State the preparation type.
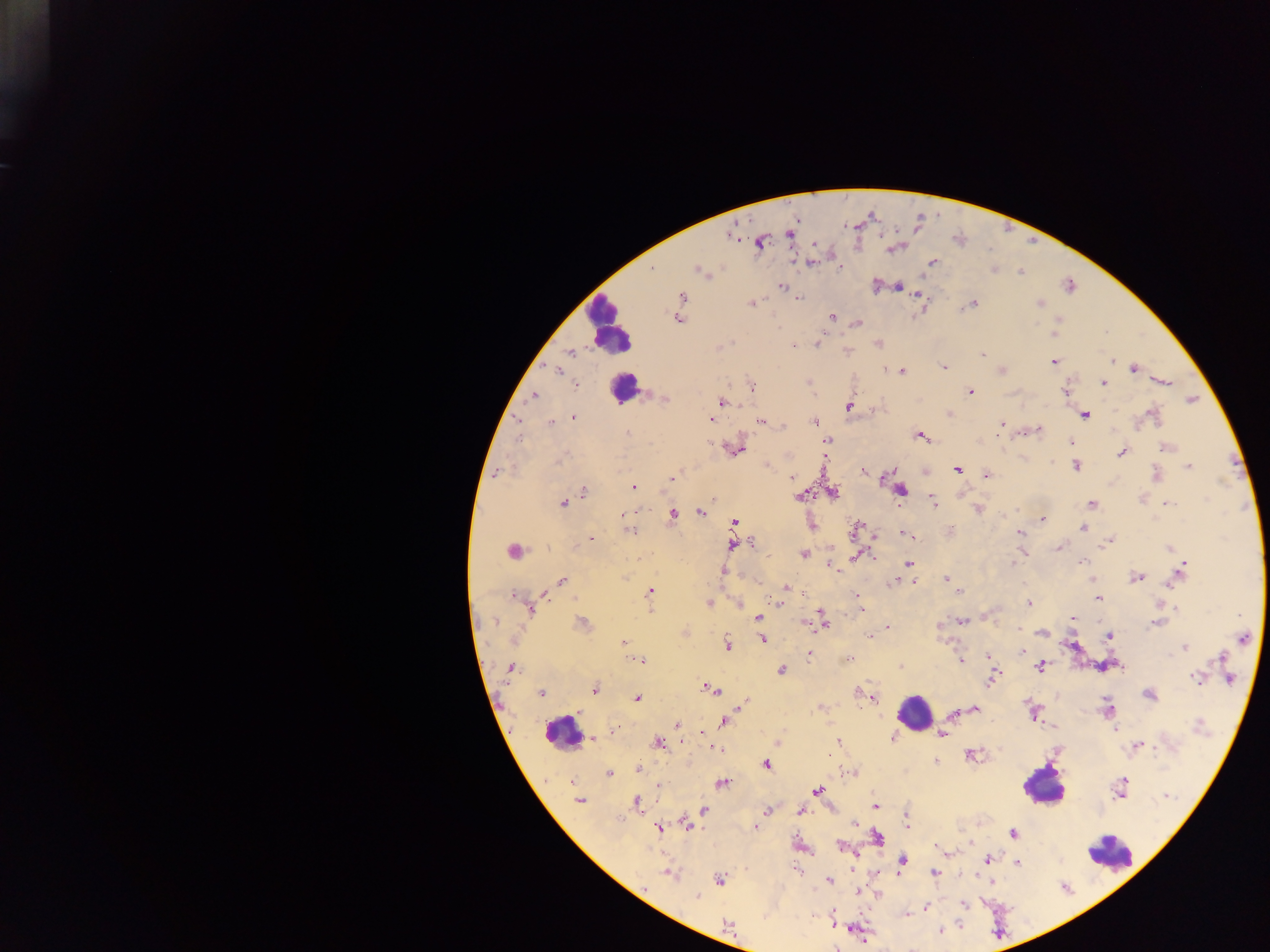

Thick blood smear.

Approximate centers as [x, y] in pixels. Leukocyte locations: [607, 325], [623, 388], [914, 711], [562, 732], [1043, 785], [1109, 852]. Plasmodium parasite locations: [730, 234], [789, 234], [760, 242], [894, 247], [809, 262], [933, 262], [838, 267], [700, 270], [1021, 272], [875, 286], [898, 286], [783, 287], [918, 295], [681, 296], [799, 298], [752, 303], [972, 304], [1040, 304], [831, 316], [678, 318], [1058, 320], [856, 322], [817, 344], [877, 344], [720, 345], [793, 346], [570, 352], [845, 353], [983, 353], [1053, 360], [1112, 360], [943, 367], [1134, 368], [557, 369], [1002, 369], [886, 370], [901, 371], [1163, 381], [1103, 383], [575, 385], [751, 385], [970, 392], [1065, 392], [533, 396], [665, 399], [1191, 399], [722, 402], [848, 406], [873, 408], [949, 414], [1084, 414], [1153, 414], [574, 417], [710, 419], [762, 421], [815, 421], [549, 422], [783, 424], [1001, 424], [1037, 429], [628, 433], [920, 436], [518, 438], [827, 440], [1070, 442], [1167, 446], [735, 448], [1122, 452], [766, 465], [1076, 466], [1188, 466], [862, 470], [958, 470], [891, 471], [924, 471], [497, 472], [1155, 474], [987, 475], [672, 478], [792, 478], [633, 487], [583, 491], [900, 491], [831, 492], [962, 492], [800, 496], [712, 498], [933, 499], [563, 502], [1166, 503], [1092, 504], [978, 509], [672, 512], [702, 512], [1042, 519], [735, 522], [810, 524], [1086, 525], [1083, 528], [629, 530], [856, 530], [950, 531], [1020, 533], [905, 535], [874, 536], [590, 538], [1107, 542], [733, 544], [751, 544], [1059, 548], [1170, 548], [513, 551], [1021, 552], [803, 554], [872, 556], [856, 557], [1079, 562], [908, 564], [1012, 565], [831, 566], [724, 571], [1181, 571], [1176, 576], [1136, 577], [947, 578], [1090, 579], [562, 580], [895, 581], [914, 581], [786, 587], [649, 591], [542, 592], [958, 592], [515, 595], [1098, 598], [778, 602], [708, 603], [738, 603], [1028, 603], [1164, 604], [529, 607], [651, 607], [1176, 607], [861, 609], [759, 617], [1072, 618], [821, 619], [961, 620], [1157, 622], [583, 623], [804, 623], [887, 628], [1019, 629], [685, 632], [1042, 632], [1108, 635], [869, 636], [1244, 637], [762, 639], [622, 642], [726, 644], [1073, 646], [1185, 647], [1021, 651], [809, 654], [987, 656], [1221, 657], [639, 660], [848, 660], [960, 660], [1039, 665], [509, 667], [900, 667], [782, 670], [994, 674], [1197, 678], [1228, 678], [594, 689], [707, 689], [541, 693], [859, 693], [1149, 694], [870, 696], [636, 697], [742, 703], [821, 707], [1107, 708], [973, 709], [578, 711], [1033, 712], [953, 715], [724, 720], [677, 725], [1115, 728], [612, 733], [702, 733], [943, 734], [893, 737], [591, 739], [836, 741], [657, 743], [776, 743], [1137, 745], [715, 748], [970, 755], [935, 762], [766, 764], [638, 768], [850, 772], [608, 773], [574, 781], [722, 782], [659, 785], [817, 790], [1119, 790], [1166, 796], [579, 799], [637, 803], [874, 805], [704, 810], [768, 810], [800, 810], [906, 814], [855, 822], [685, 824], [907, 825], [659, 827], [755, 827], [1013, 833], [877, 838], [798, 844], [970, 844], [949, 852], [851, 853], [988, 859], [901, 861], [1016, 862], [798, 870], [934, 872], [668, 873], [719, 880], [829, 880], [859, 892], [876, 893], [697, 896], [963, 904], [926, 907], [907, 915], [832, 917], [727, 924], [939, 931], [863, 938]. Photographed through a microscope with a mobile-phone camera. Image is 1270×952 pixels. Collected in Ghana. Single field of view.